Assess for parasitized red blood cells.
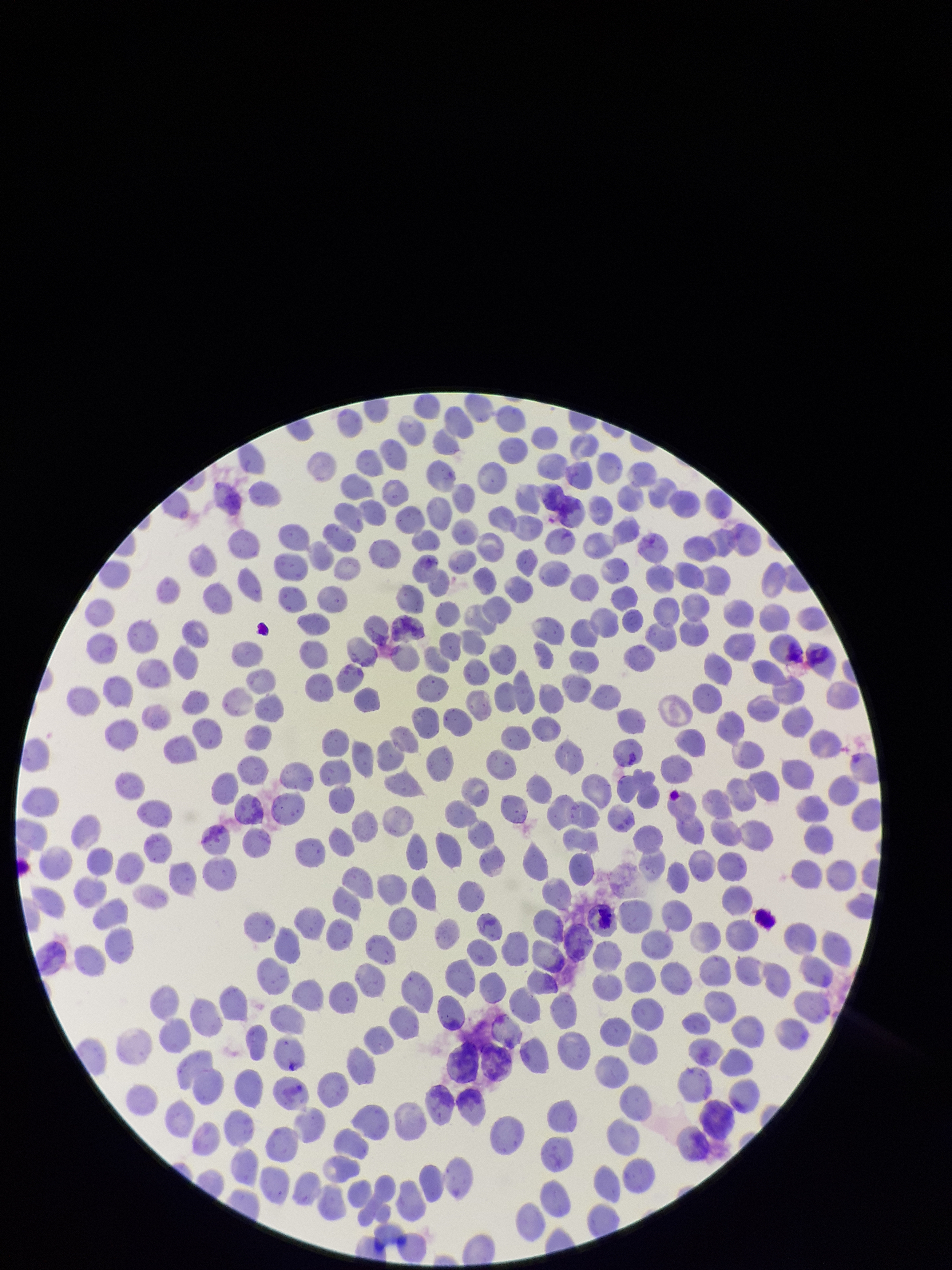

None detected.

red blood cell count = 356
preparation = thin smear
parasitized red blood cell count = 0
image size = 952×1270 pixels
stain = Giemsa
capture = smartphone photograph through the microscope eyepiece
field of view = one from this slide
patient malaria status = negative